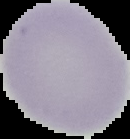
preparation: thin blood film
image_type: segmented cell region on a black background
result: no malaria parasites seen
image_size: 130×139 pixels